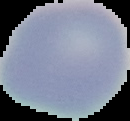
Malaria status: uninfected. Image is 130×121 pixels. The area outside the segmented cell region is set to black. From a thin blood smear.